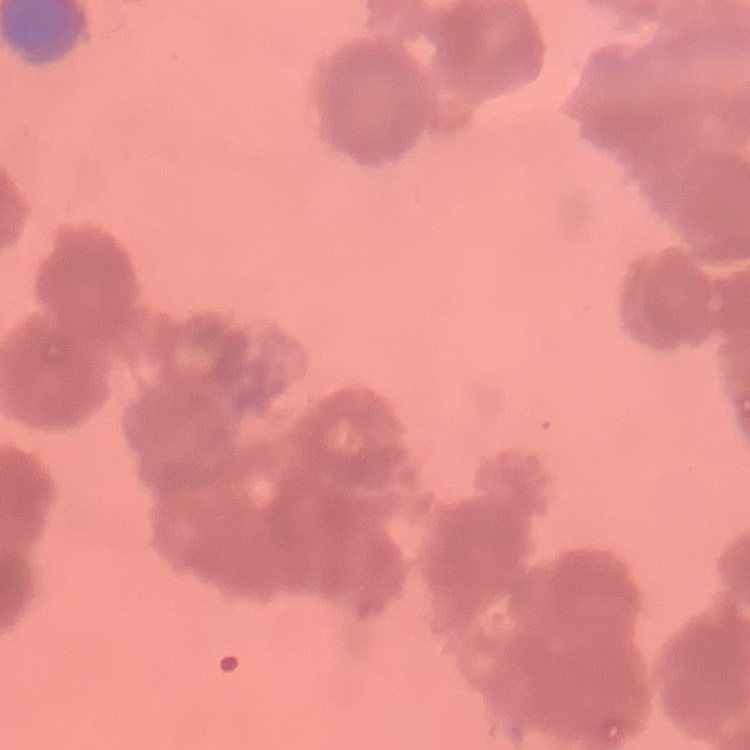
red_blood_cell_morphology: rouleaux formation
stain: Field's or Giemsa
image_type: one tile cut from a larger photomicrograph
preparation: thin blood film